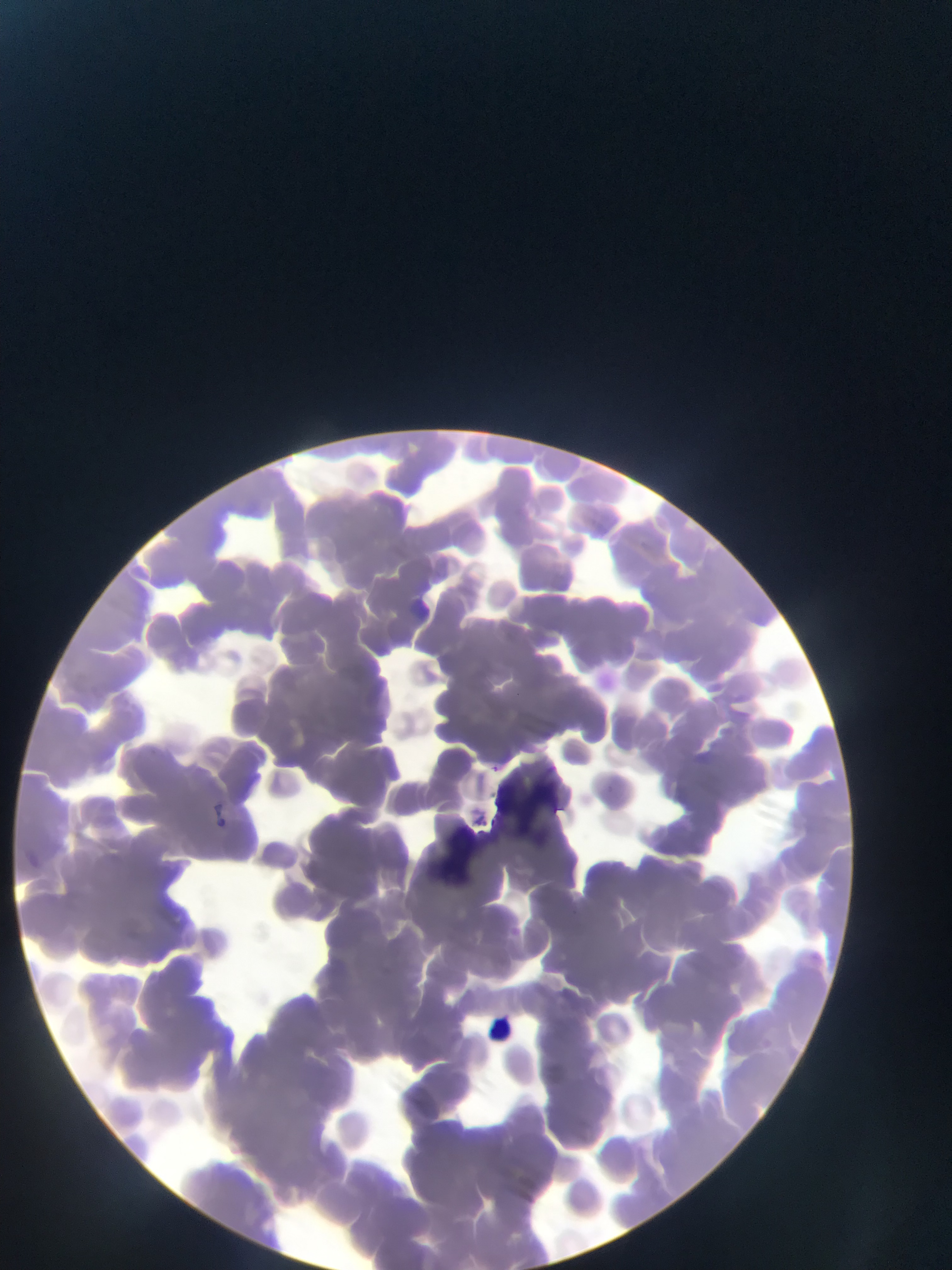

Approximate bounding boxes as [left, top, right, bottom] in pixels.
Summary:
  - Plasmodium parasite locations: [485, 762, 503, 778]
  - Leukocyte locations: [473, 1004, 546, 1070]
  - Artifact (stain precipitate or debris) locations: [506, 759, 569, 844], [451, 800, 489, 870]
  - Image size: 952×1270 pixels
  - Preparation: thin blood smear
  - Country: Ghana
  - Field of view: single
  - Capture: mobile-phone photograph through a microscope